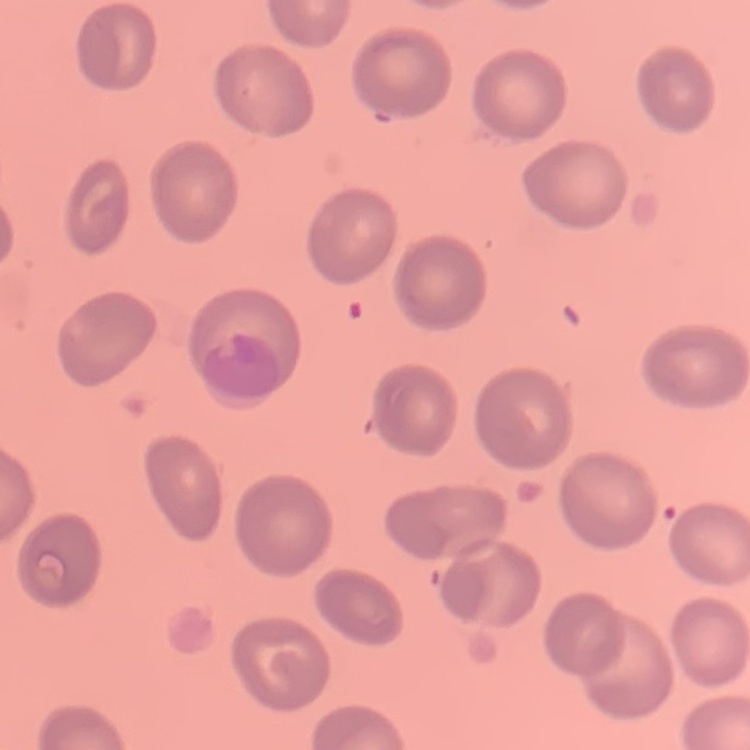
erythrocyte morphology = no rouleaux formation
preparation = thin blood film
image type = square crop of a larger photomicrograph
stain = Field's or Giemsa